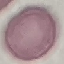

result = no malaria parasites detected
image type = cell patch, automatically extracted from a larger field of view and resized to 64 × 64 pixels
preparation = thin blood smear
capture = smartphone camera at the microscope eyepiece
stain = Giemsa